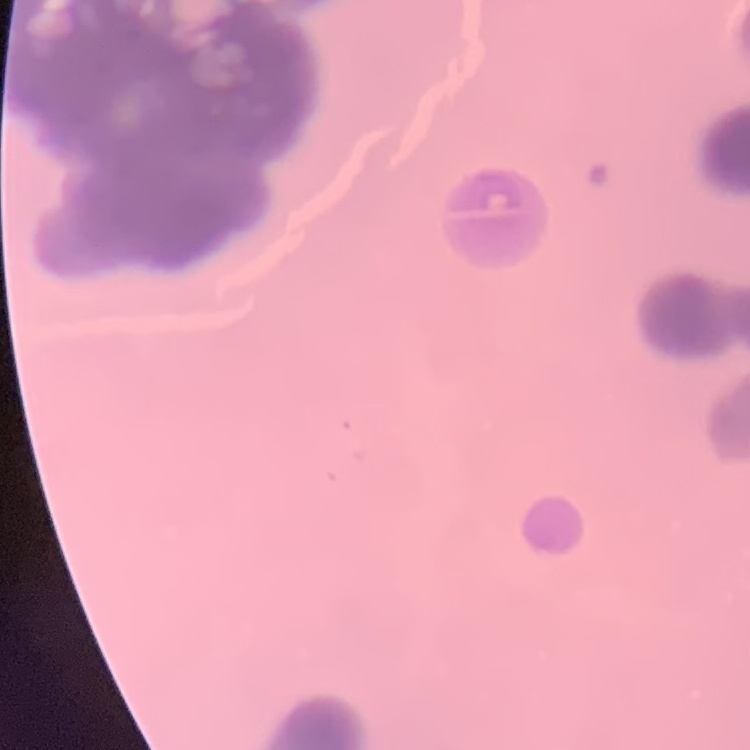

Summary:
  - Erythrocyte morphology: rouleaux formation
  - Image type: one tile cut from a larger photomicrograph
  - Stain: Field's or Giemsa
  - Preparation: thin peripheral smear